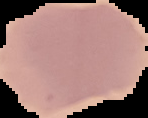
Result: no malaria parasites seen. From a thin blood film. Image is 148×118 pixels. Cell region segmented out of the field of view; the surrounding area is masked to black.